Classify the preparation.
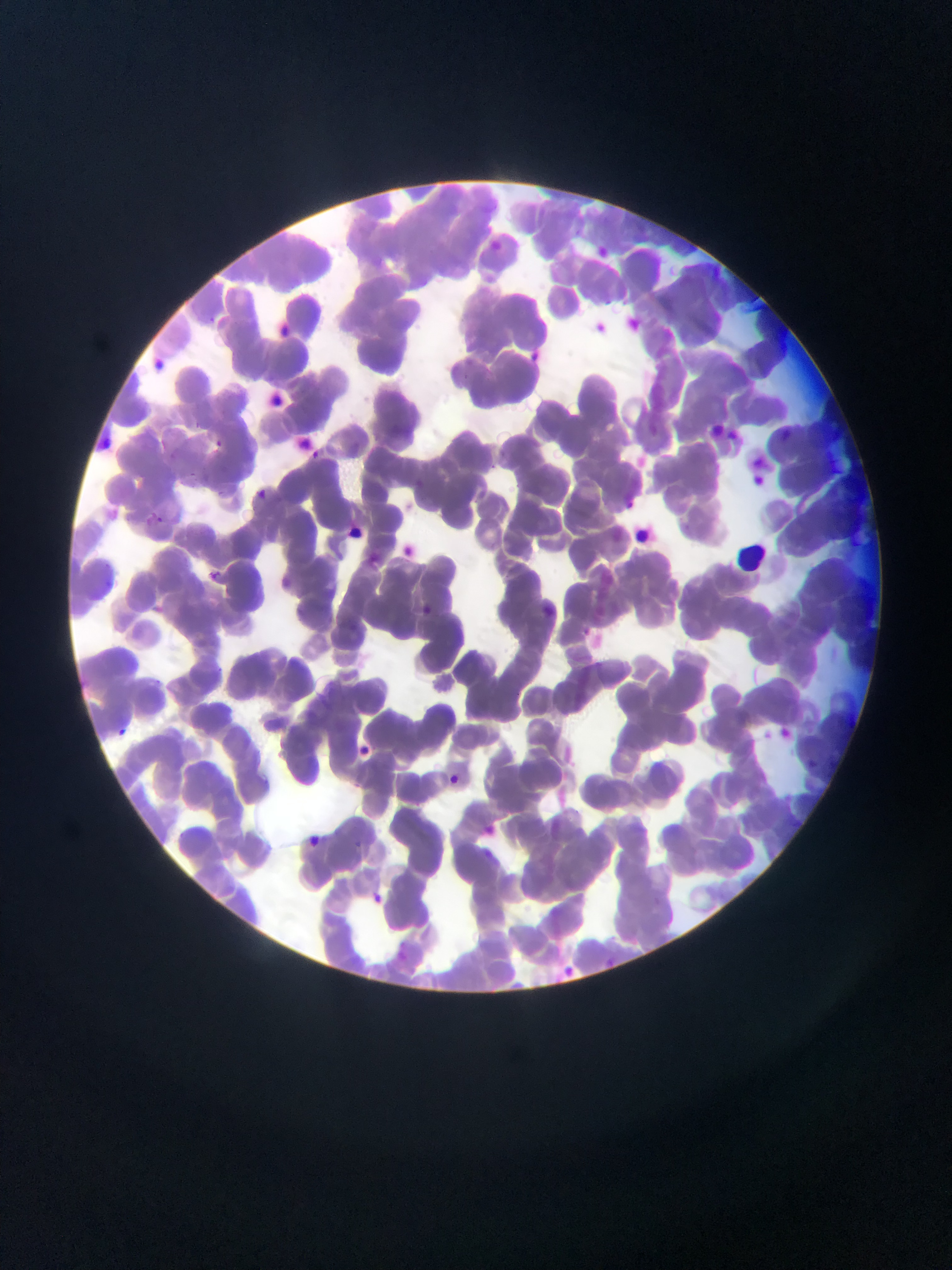
This is a thin smear.

Approximate bounding boxes as left top right bottom in pixels.
Summary:
  - Plasmodium parasite locations: 152 361 168 374; 776 427 795 448; 210 437 224 452; 305 448 322 462; 749 471 770 491; 209 487 227 501; 254 488 268 502; 144 513 165 531; 398 543 417 561; 206 567 222 582; 421 601 438 618; 585 626 594 636; 776 725 793 741; 113 726 129 742; 806 758 823 773; 444 772 463 790; 301 832 324 852; 366 888 388 909; 566 964 573 973
  - Image size: 952×1270 pixels
  - Field of view: single
  - Capture: mobile-phone photograph through a microscope
  - Country: Ghana